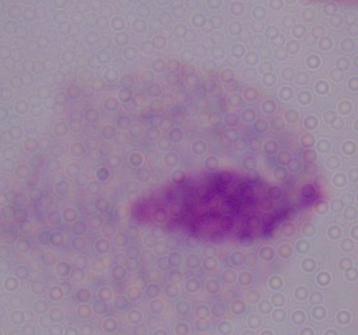
modality: photomicrograph
magnification: 1000x
identification: trichomonad